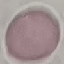
result = no malaria parasites seen
capture = smartphone camera at the microscope eyepiece
preparation = thin blood film
stain = Giemsa
image type = cell patch, automatically extracted from a larger field of view and resized to 64 × 64 pixels